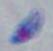

magnification = 1000x
modality = micrograph
identification = Toxoplasma gondii